Locate and identify every blood parasite.
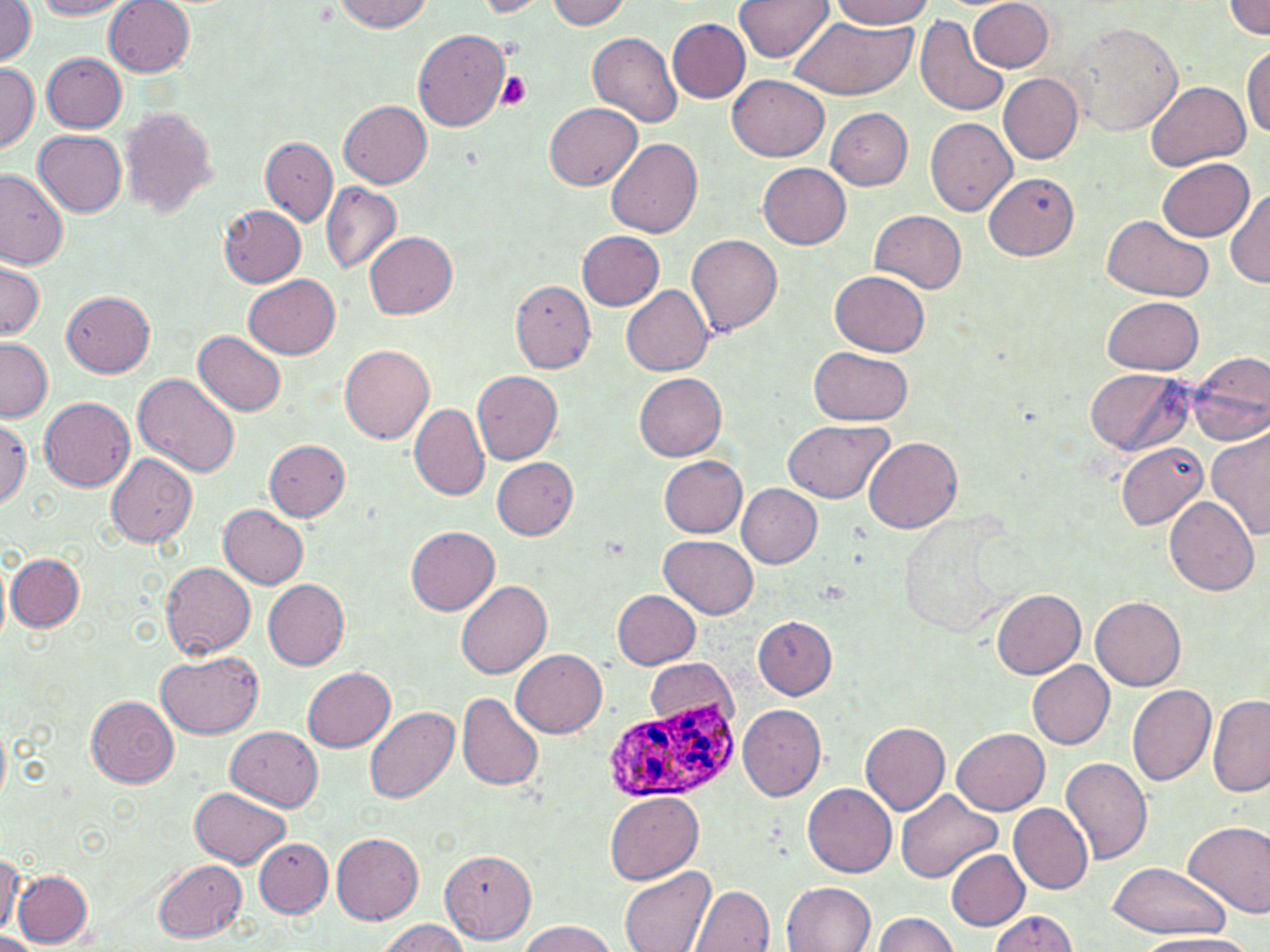
Approximate bounding boxes as (x1,y1)-(x2,y2) corner pairs in pixels.
Plasmodium ovale-infected red blood cells: (611,698)-(736,806).
No Plasmodium falciparum, Plasmodium malariae, Plasmodium vivax, Babesia divergens, or Trypanosoma brucei observed.

Summary:
  - Uninfected red blood cell locations: (35,0)-(134,18), (543,0)-(632,28), (735,0)-(832,62), (0,1)-(37,65), (332,1)-(434,32), (471,1)-(552,16), (830,1)-(932,28), (105,2)-(193,75), (971,2)-(1053,72), (1225,2)-(1270,38), (915,12)-(1009,116), (785,14)-(916,100), (668,18)-(749,102), (1065,22)-(1183,136), (413,30)-(510,131), (588,32)-(683,126), (1245,43)-(1270,140), (42,53)-(128,132), (0,63)-(38,153), (999,74)-(1083,163), (728,75)-(829,162), (1145,78)-(1251,169), (340,100)-(432,187), (545,103)-(643,192), (825,107)-(913,190), (119,108)-(217,216), (927,118)-(1017,216), (33,131)-(125,216), (260,137)-(337,227), (607,137)-(703,238), (1156,157)-(1253,242), (758,162)-(852,248), (0,168)-(68,269), (984,172)-(1079,260), (322,182)-(402,275), (1227,187)-(1269,287), (219,205)-(306,287), (869,210)-(967,293), (1103,216)-(1212,301), (364,230)-(458,318), (577,231)-(663,309), (687,234)-(782,336), (0,257)-(43,341), (830,270)-(930,356), (244,274)-(341,357), (510,280)-(595,370), (622,284)-(713,376), (62,291)-(154,376), (1103,296)-(1204,374), (195,331)-(287,416), (0,337)-(52,422), (339,341)-(434,444), (809,348)-(913,426), (1188,353)-(1270,447), (1085,368)-(1191,455), (472,370)-(562,465), (633,370)-(726,460), (133,372)-(241,478), (40,396)-(134,491), (409,403)-(490,501), (0,419)-(30,507), (783,419)-(893,504), (1207,429)-(1269,542), (865,436)-(962,532), (264,439)-(350,520), (1114,442)-(1208,531), (107,453)-(198,547), (659,456)-(747,538), (492,457)-(577,540), (738,484)-(821,567), (1164,497)-(1259,595), (219,505)-(309,588), (405,524)-(500,615), (660,535)-(758,618), (6,555)-(84,630), (161,561)-(257,659), (264,579)-(349,669), (455,579)-(553,679), (992,589)-(1086,678), (613,590)-(701,669), (1092,596)-(1187,690), (754,616)-(837,699), (512,649)-(608,738), (155,650)-(264,739), (646,659)-(734,728), (1028,661)-(1114,749), (302,667)-(396,751), (1127,684)-(1216,786), (456,693)-(544,791), (1208,693)-(1270,798), (87,695)-(180,786), (738,704)-(827,800), (363,706)-(459,803), (860,720)-(949,815), (0,725)-(10,800), (227,726)-(323,811), (953,727)-(1049,815), (1059,758)-(1152,866), (804,783)-(897,877), (190,787)-(289,868), (894,789)-(1001,883), (607,791)-(705,882), (1010,804)-(1094,893), (1184,820)-(1270,919), (332,832)-(423,925), (253,837)-(332,918), (947,850)-(1030,929), (440,851)-(536,942), (0,852)-(22,935), (154,859)-(248,941), (1105,862)-(1228,938), (619,867)-(716,952), (13,870)-(92,947), (782,882)-(875,952), (689,885)-(775,952), (990,910)-(1078,952), (870,913)-(960,951), (376,919)-(470,952), (518,920)-(616,952), (0,933)-(45,952), (1139,934)-(1260,952)
  - Platelet locations: (496,71)-(530,109)
  - Slide-level diagnosis: Plasmodium ovale
  - Field of view: one of a larger specimen
  - Image size: 1270×952 pixels
  - Modality: light microscopy
  - Preparation: thin blood film
  - Stain: May-Grünwald-Giemsa
  - Magnification: 1000x